Outline each uninfected red blood cell.
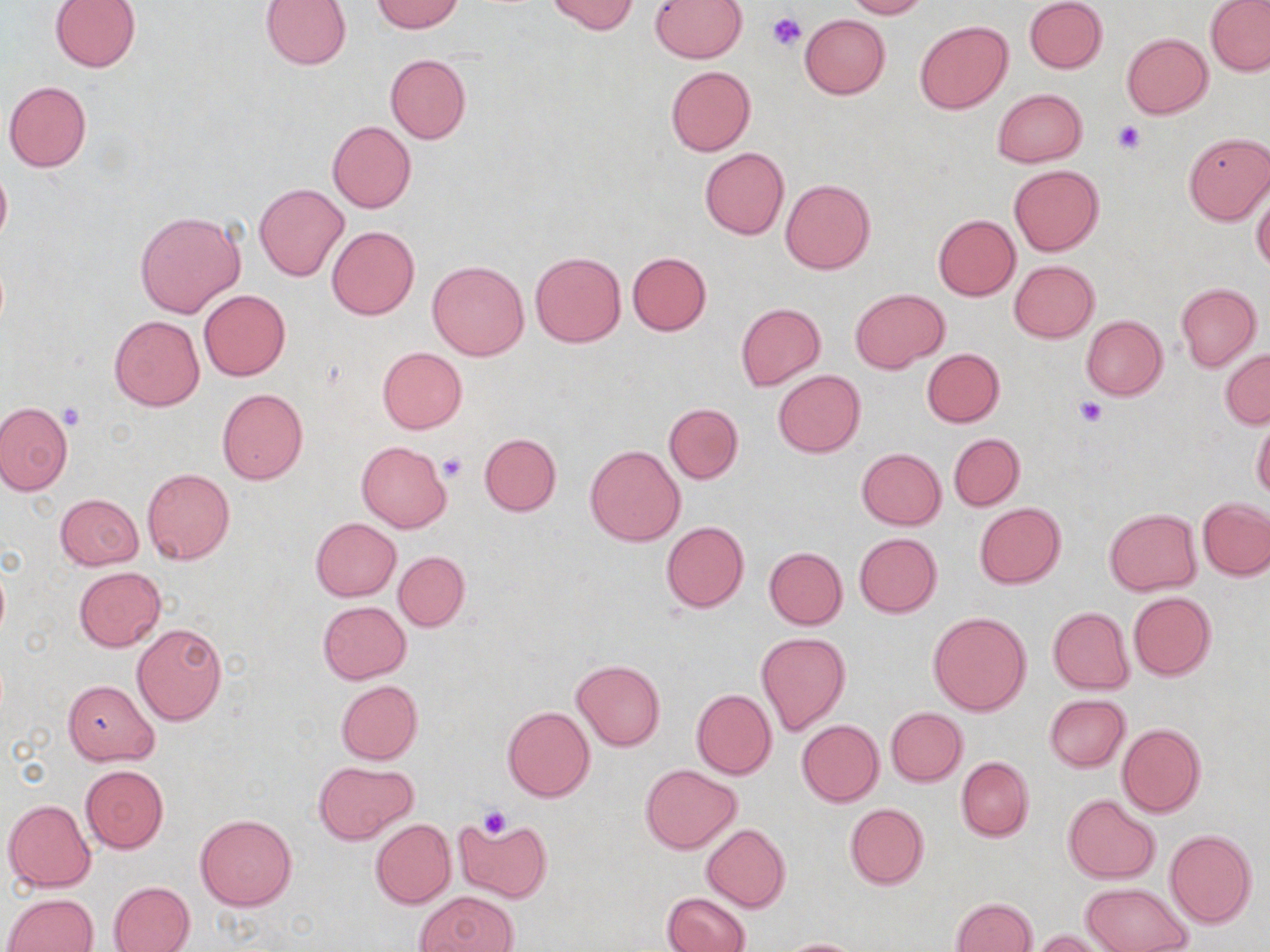
Approximate bounding boxes as [x1, y1, x2, y2] in pixels.
Uninfected red blood cells: [260, 0, 352, 69], [371, 0, 464, 33], [545, 0, 639, 34], [649, 0, 747, 61], [844, 0, 928, 19], [1024, 0, 1108, 74], [50, 1, 141, 72], [1206, 1, 1270, 76], [800, 15, 890, 99], [915, 20, 1012, 114], [1121, 32, 1211, 118], [385, 53, 471, 144], [665, 66, 756, 155], [4, 81, 92, 171], [992, 88, 1087, 167], [327, 120, 416, 213], [1182, 132, 1269, 224], [700, 147, 789, 240], [0, 162, 11, 252], [1008, 165, 1104, 255], [781, 178, 875, 274], [254, 183, 349, 282], [1252, 192, 1270, 271], [134, 209, 246, 319], [933, 215, 1021, 301], [326, 226, 420, 320], [529, 252, 626, 347], [627, 252, 712, 336], [1009, 260, 1099, 343], [428, 261, 529, 361], [1175, 283, 1261, 371], [198, 289, 290, 381], [850, 289, 948, 373], [736, 303, 826, 391], [109, 315, 204, 410], [1081, 316, 1167, 401], [377, 347, 467, 433], [1220, 347, 1270, 429], [922, 348, 1005, 427], [773, 370, 866, 457], [217, 388, 308, 485], [0, 401, 73, 495], [665, 403, 743, 484], [1252, 417, 1270, 502], [479, 433, 561, 516], [949, 433, 1025, 510], [356, 441, 452, 533], [585, 445, 685, 546], [856, 448, 946, 530], [142, 469, 235, 565], [55, 493, 144, 570], [1198, 498, 1270, 579], [974, 502, 1065, 589], [1104, 507, 1201, 596], [310, 518, 401, 601], [661, 521, 749, 612], [855, 532, 941, 617], [764, 546, 848, 629], [393, 551, 470, 631], [74, 566, 166, 652], [1128, 592, 1217, 681], [317, 600, 411, 684], [1048, 607, 1134, 695], [927, 611, 1032, 717], [132, 623, 226, 725], [755, 632, 851, 737], [572, 659, 665, 751], [62, 679, 158, 765], [336, 680, 423, 765], [691, 688, 776, 780], [1044, 694, 1129, 772], [503, 705, 595, 802], [886, 707, 967, 786], [797, 719, 884, 806], [1117, 723, 1207, 817], [955, 755, 1034, 841], [316, 760, 417, 845], [80, 764, 168, 852], [640, 764, 742, 853], [1064, 794, 1160, 883], [5, 798, 96, 892], [844, 803, 929, 889], [195, 813, 298, 910], [454, 817, 552, 903], [371, 818, 456, 909], [702, 824, 791, 912], [1165, 829, 1257, 928], [108, 881, 195, 951], [1080, 882, 1193, 952], [417, 891, 519, 952], [663, 892, 751, 952], [4, 893, 99, 952], [950, 898, 1037, 952], [1030, 929, 1117, 952], [776, 937, 869, 951].

{
  "slide_level_diagnosis": "no evidence of blood parasites",
  "modality": "optical microscopy",
  "magnification": "1000x",
  "image_size": "1270×952 pixels",
  "preparation": "thin blood film",
  "field_of_view": "one of a larger specimen",
  "platelet_locations": "approximate bounding boxes as [x1, y1, x2, y2] in pixels: [769, 12, 805, 50], [1112, 121, 1145, 154], [1075, 396, 1108, 427], [59, 403, 85, 429], [440, 454, 468, 481], [478, 805, 512, 838]",
  "stain": "May-Grünwald-Giemsa"
}